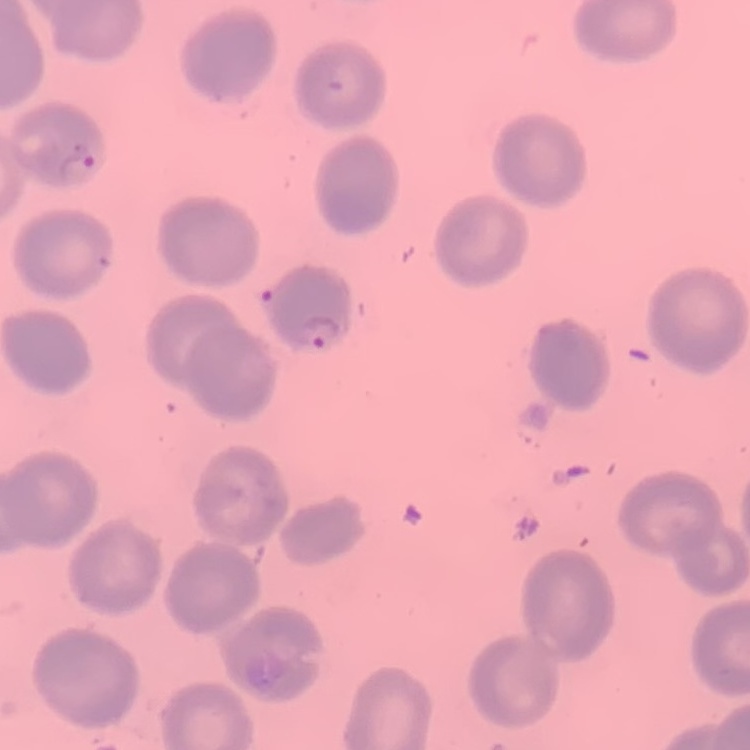

red blood cell morphology = no rouleaux formation
image type = one tile cut from a larger photomicrograph
preparation = thin peripheral smear
stain = Field's or Giemsa